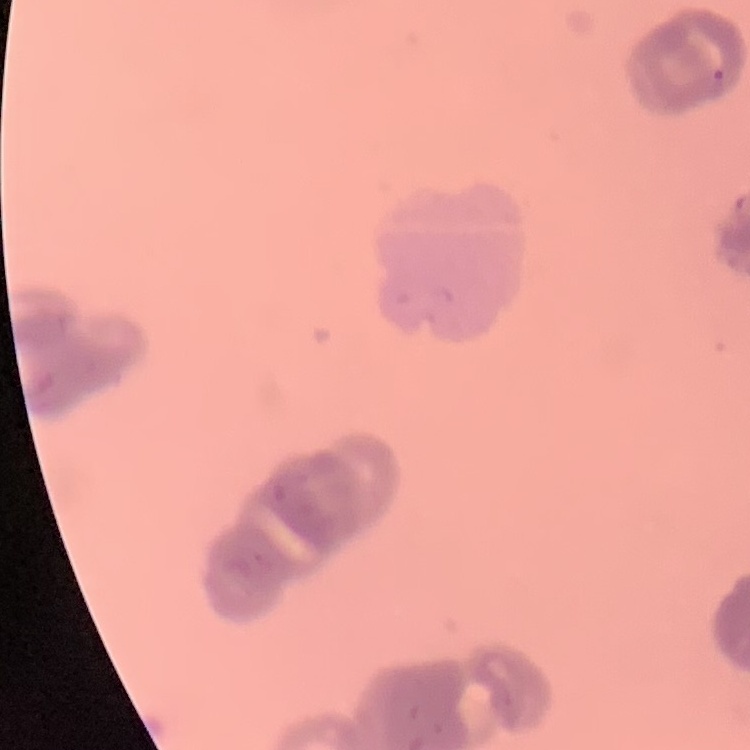
Summary:
  - Erythrocyte morphology: rouleaux formation
  - Image type: one tile cut from a larger photomicrograph
  - Preparation: thin peripheral smear
  - Stain: Field's or Giemsa